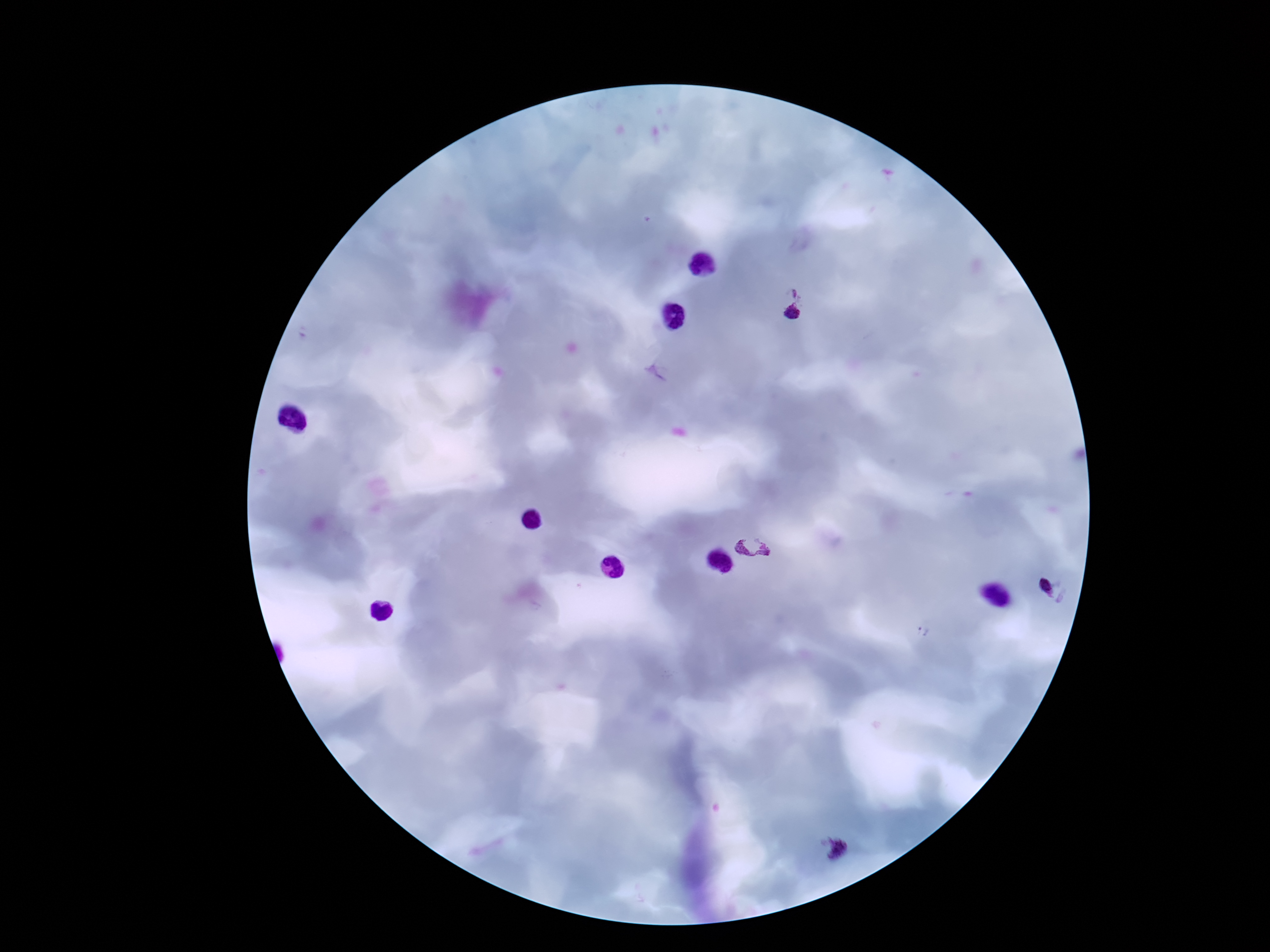

Approximate centers as (x, y) in pixels. Plasmodium parasite locations: (794, 292), (793, 314), (762, 547), (1047, 587), (922, 631), (838, 849). Thick blood film. Single field of view. 100x magnification. Photographed through the microscope eyepiece with a smartphone camera. Image is 1270×952 pixels. Patient malaria status: infected. Giemsa-stained preparation.